Give the extent of all Plasmodium vivax-infected red blood cells.
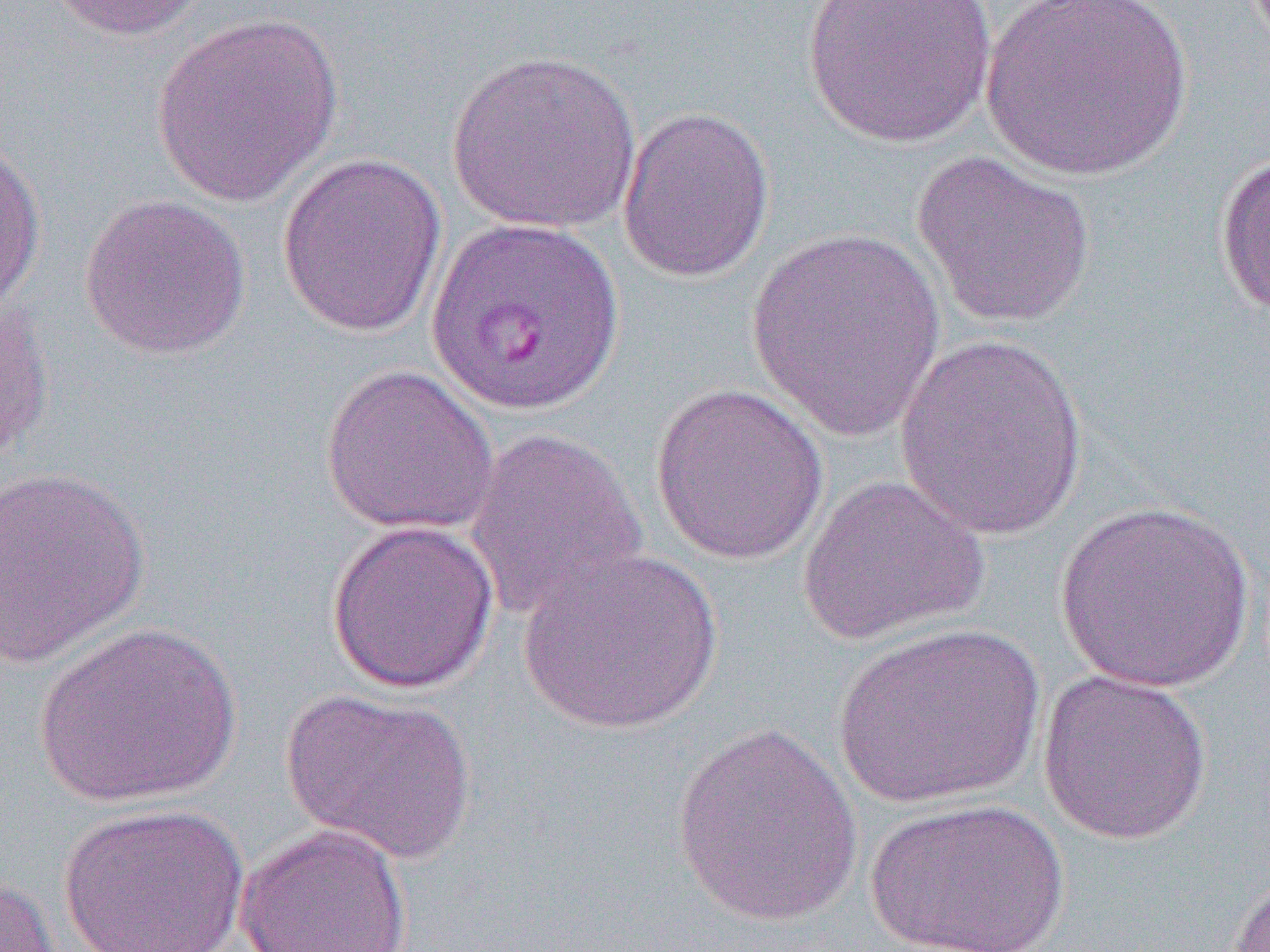
Approximate bounding boxes as (x1,y1)-(x2,y2) corner pairs in pixels.
Plasmodium vivax-infected red blood cells: (428,214)-(626,415).

Uninfected red blood cell locations: (41,0)-(208,41), (802,0)-(997,149), (980,0)-(1194,182), (151,12)-(344,207), (446,49)-(643,233), (616,105)-(776,283), (0,135)-(47,316), (911,149)-(1097,330), (275,151)-(447,338), (1214,152)-(1270,323), (78,192)-(251,361), (746,228)-(949,440), (0,300)-(56,462), (894,332)-(1091,540), (319,364)-(500,536), (650,382)-(829,565), (464,426)-(648,623), (0,465)-(151,666), (796,475)-(990,646), (1054,500)-(1257,693), (325,519)-(500,694), (518,546)-(724,736), (32,621)-(242,808), (833,622)-(1045,808), (1037,669)-(1213,845), (278,688)-(477,864), (670,721)-(865,927), (864,797)-(1072,952), (58,803)-(249,952), (235,823)-(412,952), (1227,868)-(1270,952), (0,873)-(63,951). Slide-level diagnosis: Plasmodium vivax. Single field of view. 1000x magnification. Thin blood smear. Optical microscopy. Image is 1270×952 pixels.